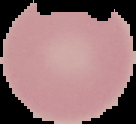
Summary:
  - Result: no malaria parasites detected
  - Preparation: thin blood smear
  - Image type: cell region segmented out of the field of view; surrounding area masked to black
  - Image size: 136×124 pixels